Identify the cell.
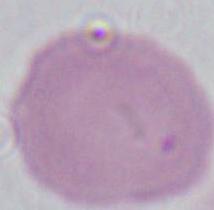

An erythrocyte.

1000x magnification. Photomicrograph.